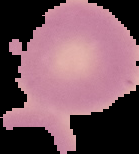
image type = cell region segmented out of the field of view; surrounding area masked to black
image size = 139×154 pixels
preparation = thin blood smear
result = negative for Plasmodium parasites